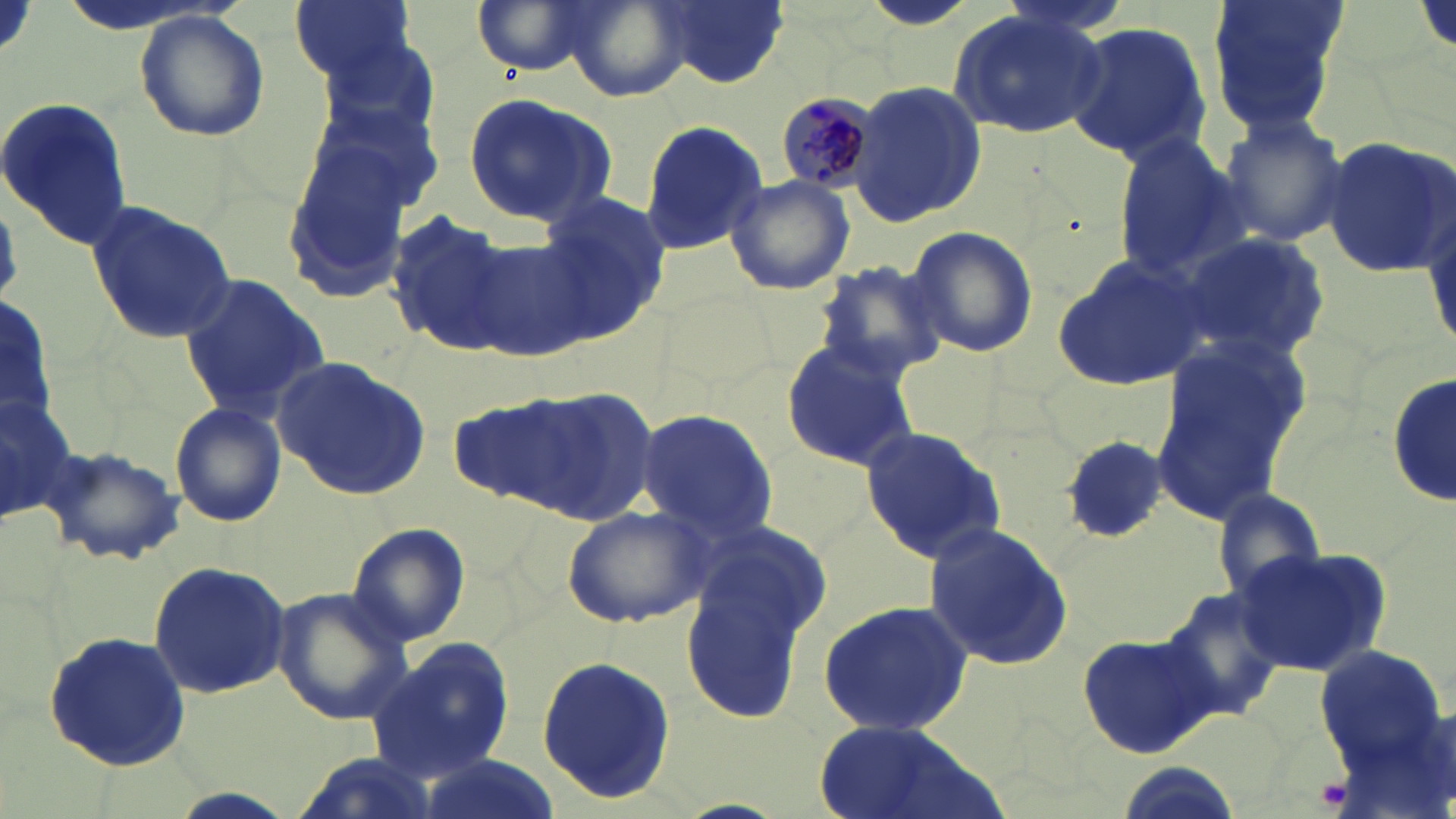

Approximate bounding boxes as (x1, y1, x2, y2) in pixels. Uninfected red blood cell locations: (289, 0, 416, 83), (469, 0, 604, 76), (649, 0, 789, 89), (992, 0, 1142, 36), (1205, 0, 1349, 137), (948, 8, 1112, 137), (133, 10, 269, 142), (1061, 20, 1211, 165), (848, 80, 986, 226), (462, 91, 616, 228), (0, 97, 132, 250), (1214, 113, 1350, 251), (636, 120, 769, 256), (1111, 132, 1248, 277), (1320, 137, 1455, 278), (280, 148, 418, 309), (725, 172, 857, 296), (537, 190, 673, 334), (83, 199, 238, 345), (385, 210, 515, 357), (904, 225, 1039, 360), (1174, 233, 1331, 363), (467, 239, 592, 361), (1051, 253, 1211, 392), (808, 258, 951, 384), (178, 273, 331, 419), (0, 290, 59, 432), (780, 335, 917, 470), (1153, 335, 1308, 525), (274, 357, 432, 500), (1388, 373, 1454, 509), (508, 385, 661, 527), (0, 386, 76, 526), (169, 401, 286, 527), (636, 407, 780, 542), (859, 427, 1007, 561), (1060, 436, 1167, 543), (41, 445, 184, 566), (1212, 490, 1324, 601), (561, 506, 711, 629), (691, 516, 834, 644), (921, 521, 1074, 674), (345, 522, 471, 647), (1234, 547, 1392, 679), (145, 558, 291, 698), (681, 563, 817, 725), (1160, 585, 1291, 724), (272, 586, 411, 725), (816, 601, 974, 736), (42, 630, 193, 769), (1077, 630, 1219, 760), (368, 637, 516, 782), (1312, 640, 1447, 783), (536, 653, 676, 804), (810, 721, 991, 819). Plasmodium malariae-infected red blood cell locations: (774, 88, 886, 192). Platelet locations: (1315, 776, 1351, 811). Slide-level diagnosis: Plasmodium malariae. 1000x magnification. Thin blood film. May-Grünwald-Giemsa stain. Image is 1456×819 pixels. Optical microscopy. Single field of view.